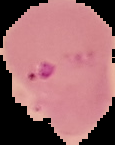

Summary:
  - Preparation: thin blood smear
  - Image type: segmented cell region with the area outside set to black
  - Image size: 115×145 pixels
  - Malaria status: parasitized